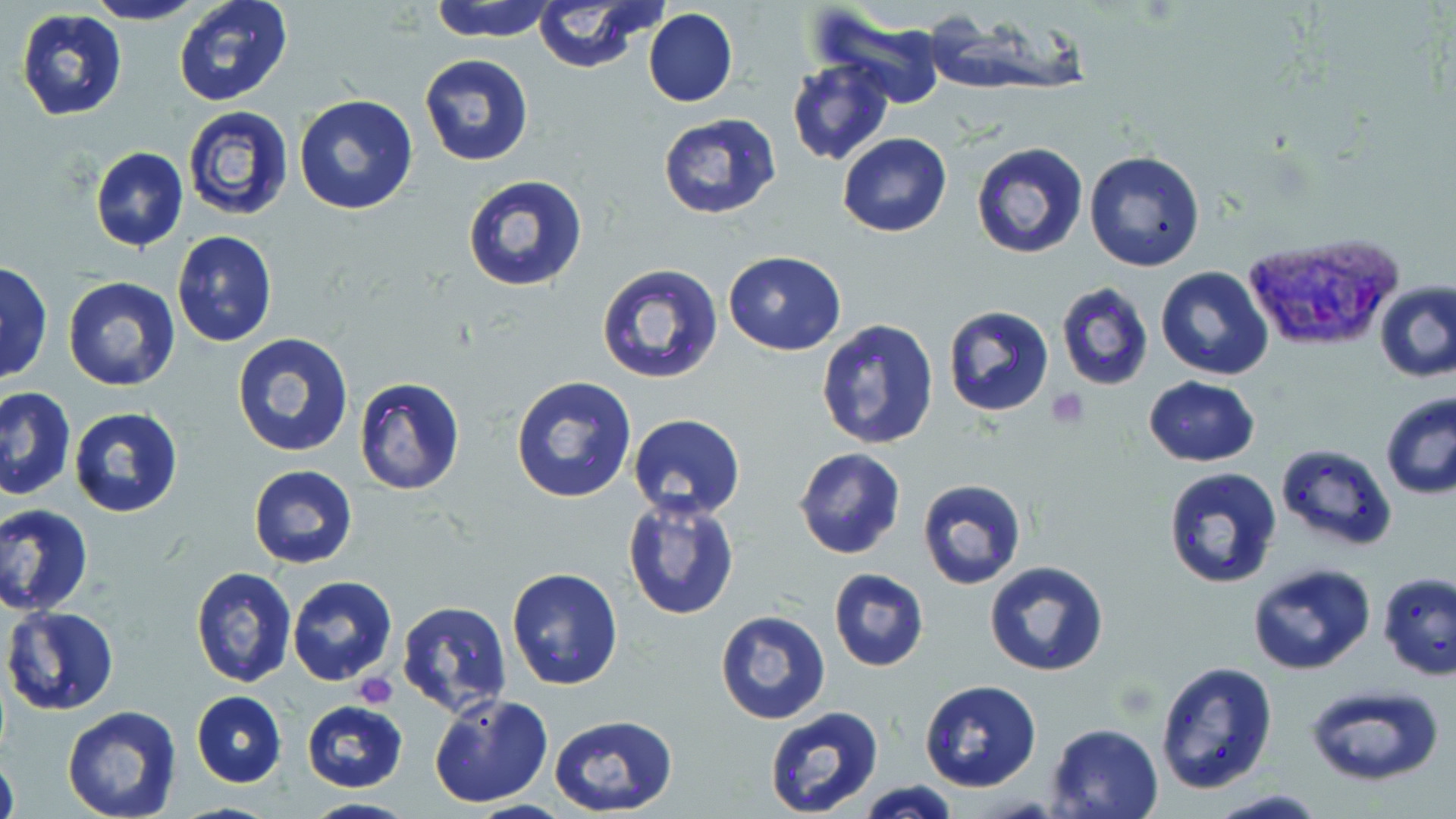
Summary:
  - Coordinate format: approximate bounding boxes as named x1/y1/x2/y2 corners in pixels
  - Platelet locations: (x1=1049, y1=389, x2=1090, y2=426), (x1=354, y1=672, x2=399, y2=708)
  - Plasmodium vivax-infected red blood cell locations: (x1=1241, y1=231, x2=1407, y2=355)
  - Uninfected red blood cell locations: (x1=84, y1=0, x2=206, y2=26), (x1=173, y1=0, x2=292, y2=107), (x1=429, y1=0, x2=559, y2=43), (x1=530, y1=0, x2=665, y2=74), (x1=807, y1=4, x2=952, y2=106), (x1=15, y1=7, x2=127, y2=121), (x1=643, y1=9, x2=737, y2=107), (x1=419, y1=53, x2=535, y2=167), (x1=786, y1=58, x2=894, y2=167), (x1=293, y1=95, x2=419, y2=216), (x1=182, y1=105, x2=296, y2=223), (x1=656, y1=111, x2=783, y2=220), (x1=837, y1=132, x2=953, y2=238), (x1=970, y1=142, x2=1087, y2=260), (x1=89, y1=146, x2=188, y2=250), (x1=1084, y1=150, x2=1206, y2=272), (x1=461, y1=173, x2=589, y2=293), (x1=172, y1=231, x2=277, y2=347), (x1=723, y1=250, x2=847, y2=355), (x1=596, y1=262, x2=723, y2=385), (x1=0, y1=264, x2=52, y2=386), (x1=1156, y1=267, x2=1273, y2=380), (x1=62, y1=276, x2=180, y2=390), (x1=1375, y1=281, x2=1456, y2=383), (x1=1056, y1=283, x2=1153, y2=391), (x1=941, y1=305, x2=1054, y2=418), (x1=815, y1=318, x2=941, y2=450), (x1=232, y1=332, x2=354, y2=457), (x1=510, y1=375, x2=638, y2=505), (x1=1143, y1=376, x2=1260, y2=467), (x1=354, y1=377, x2=465, y2=495), (x1=0, y1=385, x2=75, y2=501), (x1=1380, y1=392, x2=1456, y2=501), (x1=69, y1=405, x2=184, y2=518), (x1=626, y1=413, x2=745, y2=520), (x1=1276, y1=443, x2=1398, y2=551), (x1=793, y1=448, x2=907, y2=560), (x1=248, y1=465, x2=358, y2=567), (x1=1163, y1=467, x2=1284, y2=589), (x1=915, y1=477, x2=1026, y2=590), (x1=622, y1=494, x2=741, y2=621), (x1=0, y1=503, x2=94, y2=615), (x1=983, y1=560, x2=1109, y2=676), (x1=1247, y1=562, x2=1377, y2=677), (x1=190, y1=567, x2=296, y2=687), (x1=506, y1=567, x2=623, y2=690), (x1=828, y1=568, x2=929, y2=671), (x1=1378, y1=573, x2=1456, y2=681), (x1=287, y1=575, x2=397, y2=685), (x1=395, y1=600, x2=516, y2=719), (x1=3, y1=606, x2=121, y2=714), (x1=715, y1=611, x2=832, y2=725), (x1=1154, y1=661, x2=1278, y2=795), (x1=918, y1=680, x2=1041, y2=792), (x1=1301, y1=684, x2=1447, y2=787), (x1=191, y1=691, x2=286, y2=786), (x1=429, y1=693, x2=551, y2=808), (x1=300, y1=700, x2=409, y2=793), (x1=62, y1=706, x2=181, y2=819), (x1=763, y1=708, x2=886, y2=819), (x1=548, y1=714, x2=677, y2=817), (x1=1044, y1=722, x2=1166, y2=818), (x1=0, y1=748, x2=19, y2=819), (x1=851, y1=780, x2=964, y2=819), (x1=1205, y1=789, x2=1332, y2=819), (x1=300, y1=796, x2=417, y2=817)
  - Slide-level diagnosis: Plasmodium vivax
  - Image size: 1456×819 pixels
  - Stain: May-Grünwald-Giemsa
  - Modality: optical microscopy
  - Preparation: thin blood film
  - Field of view: one of a larger specimen
  - Magnification: 1000x